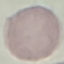
Summary:
  - Result: no malaria parasites seen
  - Stain: Giemsa
  - Capture: smartphone camera at the microscope eyepiece
  - Preparation: thin smear
  - Image type: cell patch, automatically extracted from a larger field of view and resized to 64 × 64 pixels